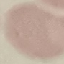
Summary:
  - Malaria status: uninfected
  - Capture: smartphone through the microscope eyepiece
  - Stain: Giemsa
  - Preparation: thin blood film
  - Image type: automatically extracted cell patch, resized to 64 × 64 pixels